Give the extent of all Plasmodium vivax-infected red blood cells.
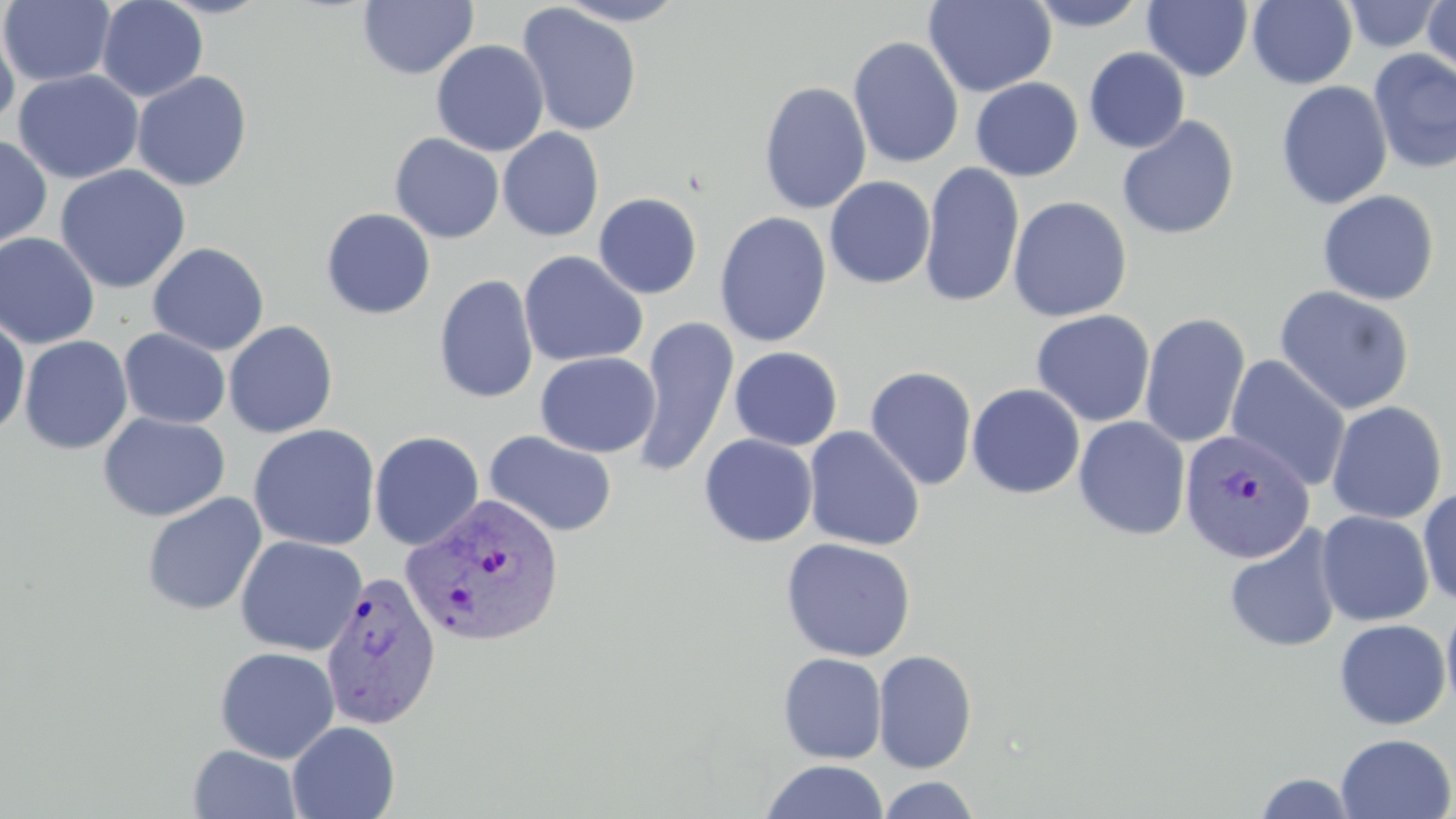

Approximate bounding boxes as named x1/y1/x2/y2 corners in pixels.
Plasmodium vivax-infected red blood cells: (x1=1179, y1=430, x2=1315, y2=563), (x1=400, y1=493, x2=565, y2=648), (x1=319, y1=570, x2=442, y2=730).

Uninfected red blood cell locations: (x1=1, y1=0, x2=116, y2=87), (x1=96, y1=0, x2=208, y2=102), (x1=552, y1=0, x2=691, y2=26), (x1=923, y1=0, x2=1057, y2=97), (x1=1247, y1=0, x2=1358, y2=89), (x1=1422, y1=0, x2=1455, y2=77), (x1=358, y1=1, x2=478, y2=80), (x1=1025, y1=1, x2=1151, y2=32), (x1=1143, y1=1, x2=1254, y2=81), (x1=1341, y1=1, x2=1446, y2=53), (x1=516, y1=3, x2=642, y2=137), (x1=0, y1=15, x2=20, y2=132), (x1=848, y1=36, x2=964, y2=169), (x1=431, y1=39, x2=549, y2=157), (x1=1084, y1=47, x2=1190, y2=153), (x1=1367, y1=49, x2=1456, y2=174), (x1=13, y1=69, x2=144, y2=184), (x1=132, y1=71, x2=253, y2=191), (x1=970, y1=77, x2=1083, y2=181), (x1=758, y1=81, x2=872, y2=215), (x1=1275, y1=81, x2=1393, y2=211), (x1=1116, y1=115, x2=1240, y2=240), (x1=498, y1=127, x2=604, y2=242), (x1=389, y1=132, x2=505, y2=243), (x1=0, y1=134, x2=53, y2=251), (x1=920, y1=161, x2=1025, y2=308), (x1=54, y1=164, x2=192, y2=294), (x1=824, y1=175, x2=935, y2=288), (x1=1317, y1=190, x2=1440, y2=306), (x1=593, y1=193, x2=702, y2=299), (x1=1007, y1=196, x2=1132, y2=322), (x1=320, y1=207, x2=436, y2=319), (x1=714, y1=211, x2=832, y2=347), (x1=0, y1=232, x2=100, y2=350), (x1=147, y1=242, x2=269, y2=356), (x1=518, y1=251, x2=648, y2=368), (x1=433, y1=274, x2=539, y2=404), (x1=1274, y1=285, x2=1415, y2=415), (x1=1031, y1=309, x2=1155, y2=427), (x1=1139, y1=313, x2=1251, y2=449), (x1=0, y1=315, x2=31, y2=438), (x1=632, y1=316, x2=739, y2=478), (x1=223, y1=320, x2=338, y2=438), (x1=118, y1=328, x2=231, y2=429), (x1=19, y1=335, x2=133, y2=455), (x1=729, y1=346, x2=843, y2=451), (x1=535, y1=352, x2=660, y2=458), (x1=1225, y1=355, x2=1351, y2=492), (x1=864, y1=366, x2=978, y2=491), (x1=966, y1=383, x2=1085, y2=499), (x1=1326, y1=401, x2=1447, y2=524), (x1=98, y1=413, x2=230, y2=522), (x1=1073, y1=416, x2=1191, y2=540), (x1=248, y1=424, x2=381, y2=551), (x1=803, y1=425, x2=925, y2=552), (x1=369, y1=430, x2=485, y2=550), (x1=484, y1=430, x2=618, y2=538), (x1=699, y1=434, x2=818, y2=547), (x1=1417, y1=488, x2=1456, y2=605), (x1=142, y1=492, x2=267, y2=617), (x1=1315, y1=510, x2=1434, y2=627), (x1=1222, y1=524, x2=1343, y2=654), (x1=234, y1=535, x2=368, y2=656), (x1=780, y1=537, x2=916, y2=663), (x1=1441, y1=600, x2=1456, y2=720), (x1=1333, y1=619, x2=1452, y2=730), (x1=214, y1=646, x2=339, y2=763), (x1=873, y1=650, x2=977, y2=773), (x1=777, y1=652, x2=887, y2=764), (x1=287, y1=721, x2=400, y2=819), (x1=1335, y1=733, x2=1455, y2=818), (x1=188, y1=744, x2=302, y2=819), (x1=759, y1=760, x2=891, y2=819), (x1=1252, y1=772, x2=1360, y2=818), (x1=877, y1=776, x2=979, y2=818). Slide-level diagnosis: Plasmodium vivax. Image is 1456×819 pixels. May-Grünwald-Giemsa stain. Light microscopy. 1000x magnification. One field of a larger specimen. Thin blood film.